Identify the parasite.
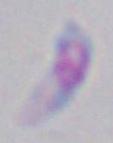
This is Toxoplasma gondii.

Summary:
  - Modality: micrograph
  - Magnification: 1000x